Name the parasite shown.
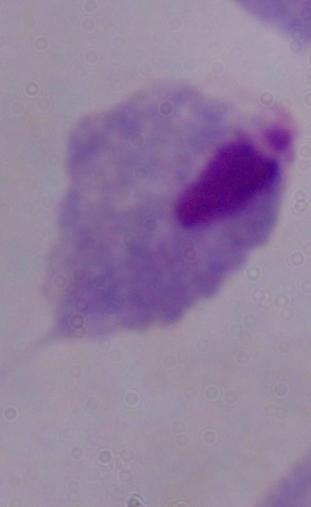

A trichomonad.

Captured at 1000x magnification. Micrograph.